Locate every malaria parasite.
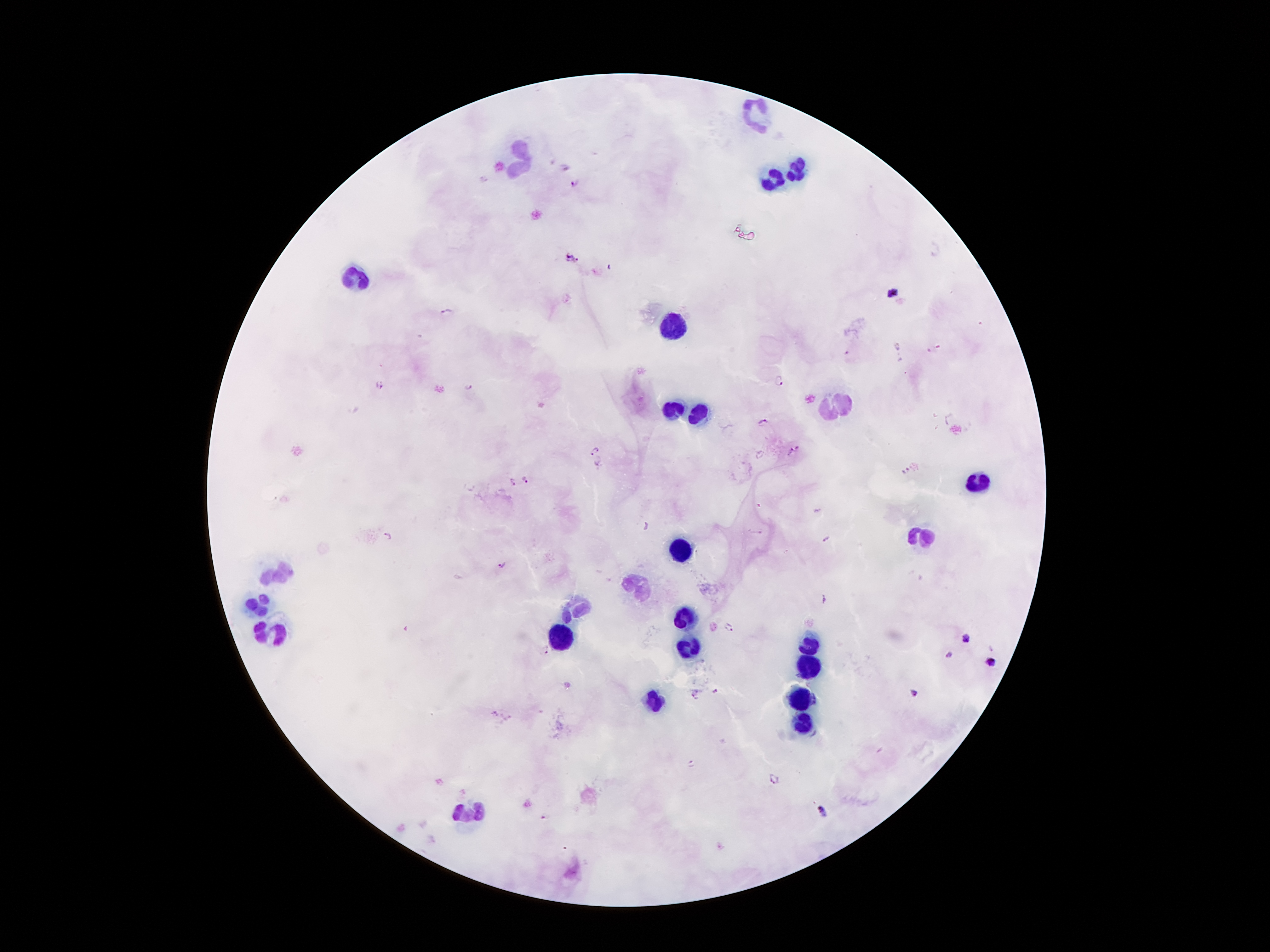
Approximate centers as {x, y} in pixels.
Malaria parasites: {566, 166}, {484, 179}, {576, 183}, {573, 257}, {893, 292}, {448, 311}, {847, 353}, {778, 380}, {381, 386}, {469, 386}, {763, 421}, {795, 450}, {594, 452}, {906, 471}, {525, 478}, {511, 482}, {646, 526}, {758, 533}, {387, 534}, {826, 539}, {505, 565}, {824, 601}, {729, 626}, {965, 640}, {547, 651}, {950, 654}, {992, 662}, {715, 689}, {915, 692}, {695, 694}, {495, 713}, {692, 763}, {773, 777}, {823, 812}, {544, 818}.

Leukocyte locations: {758, 115}, {524, 159}, {796, 171}, {773, 180}, {356, 284}, {672, 324}, {671, 411}, {700, 411}, {979, 480}, {920, 538}, {682, 546}, {284, 569}, {641, 585}, {259, 600}, {579, 604}, {684, 617}, {274, 627}, {560, 637}, {811, 645}, {691, 646}, {811, 664}, {801, 696}, {654, 701}, {806, 727}, {472, 813}. Patient malaria status: infected with Plasmodium falciparum. Thick blood film. Smartphone photograph taken through the microscope eyepiece. Single field of view. Image is 1270×952 pixels. Giemsa stain. 100x magnification.